Identify the parasite.
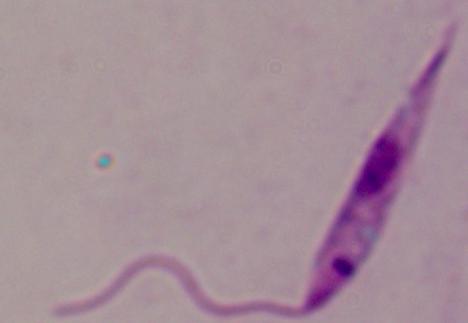
Leishmania.

1000x magnification. Photomicrograph.